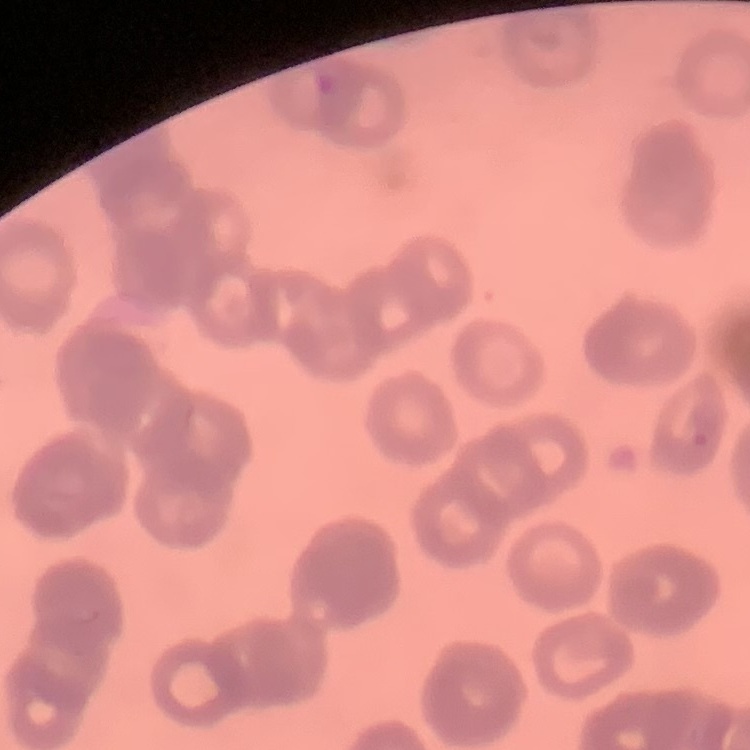 The red blood cells exhibit rouleaux formation. One tile cut from a larger photomicrograph. Field's or Giemsa stain. Thin blood smear.